State which parasite is depicted.
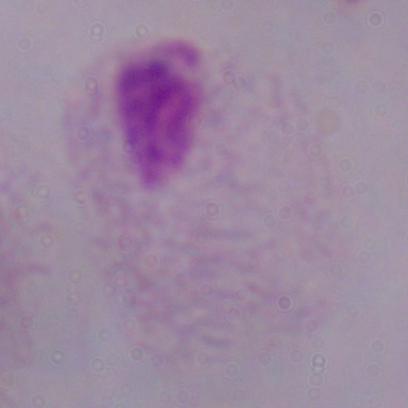
This is a trichomonad.

Summary:
  - Magnification: 1000x
  - Modality: photomicrograph